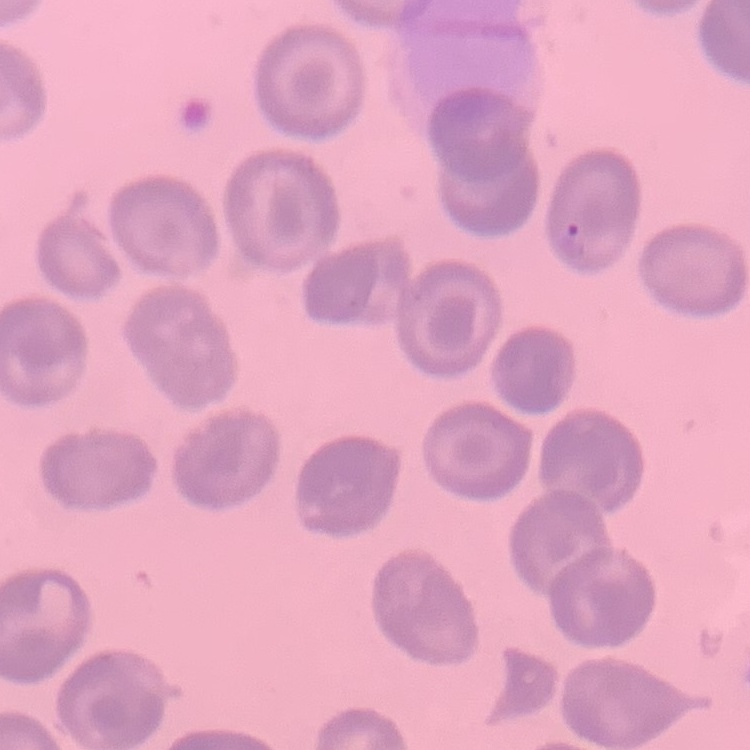
{
  "red_blood_cell_morphology": "no rouleaux formation",
  "image_type": "one tile cut from a larger photomicrograph",
  "stain": "Field's or Giemsa",
  "preparation": "thin blood smear"
}